Outline each Plasmodium malariae-infected red blood cell.
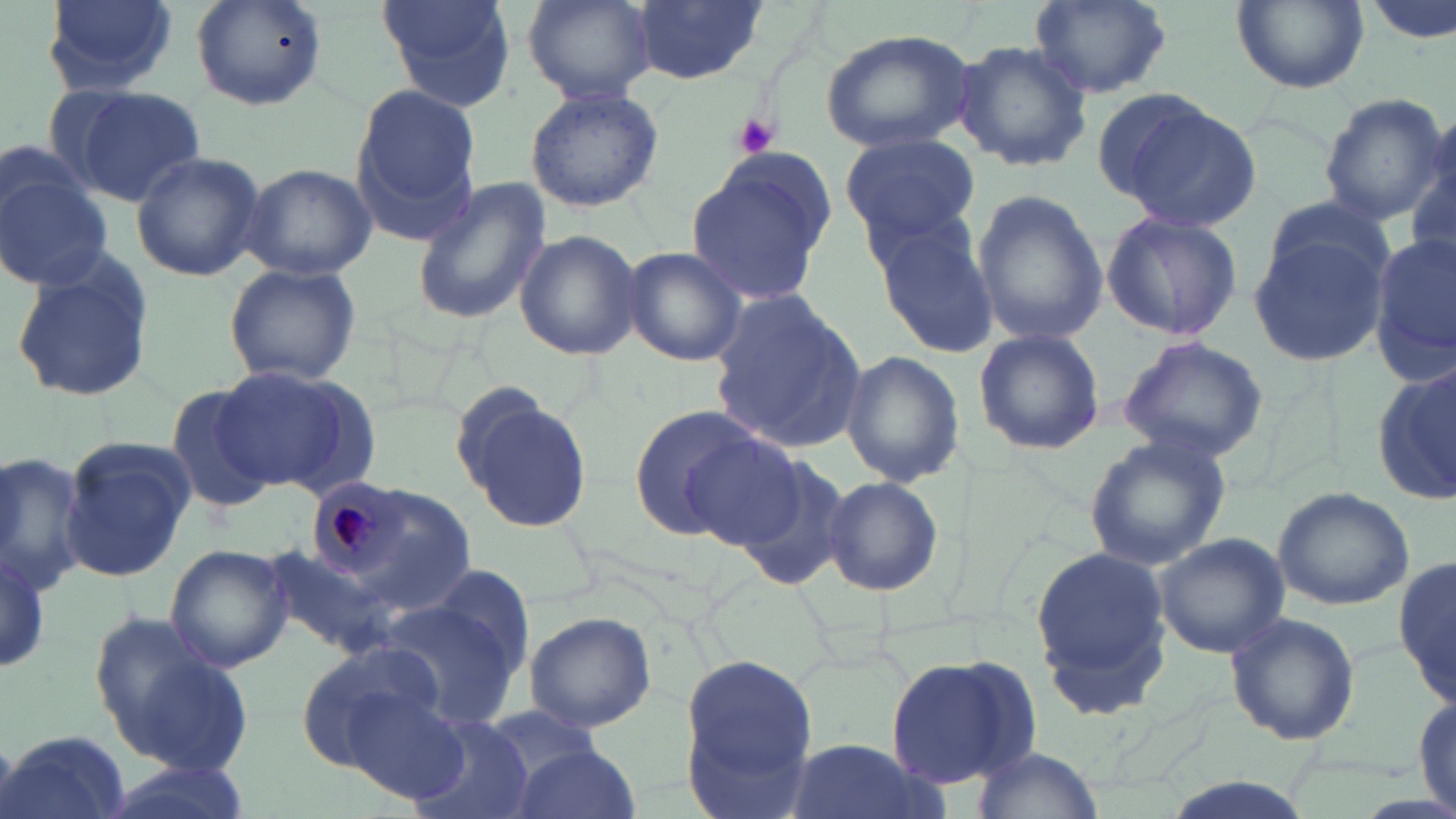
Approximate bounding boxes as [x1, y1, x2, y2] in pixels.
Plasmodium malariae-infected red blood cells: [306, 476, 409, 578].

Uninfected red blood cell locations: [39, 0, 183, 95], [187, 0, 330, 112], [376, 0, 515, 111], [522, 0, 655, 104], [630, 0, 766, 84], [1029, 0, 1171, 98], [1231, 0, 1366, 94], [1365, 0, 1456, 48], [819, 28, 977, 153], [952, 40, 1093, 173], [350, 83, 479, 244], [64, 84, 206, 207], [524, 86, 665, 213], [1316, 91, 1446, 226], [1113, 96, 1262, 231], [842, 132, 981, 242], [1410, 133, 1456, 267], [130, 151, 267, 283], [0, 152, 115, 292], [684, 162, 829, 309], [241, 164, 377, 280], [410, 177, 552, 327], [968, 187, 1108, 349], [1101, 210, 1243, 342], [866, 211, 998, 358], [1247, 218, 1391, 367], [512, 229, 642, 361], [1370, 234, 1456, 376], [621, 245, 748, 365], [9, 253, 155, 406], [222, 262, 363, 389], [709, 291, 869, 454], [973, 328, 1106, 457], [1115, 335, 1273, 463], [839, 350, 965, 487], [1373, 361, 1455, 507], [213, 366, 375, 497], [159, 384, 283, 513], [453, 385, 595, 534], [628, 404, 778, 541], [678, 431, 809, 550], [1083, 433, 1233, 572], [60, 438, 194, 582], [0, 448, 91, 598], [734, 456, 855, 593], [821, 475, 944, 597], [1270, 486, 1414, 611], [342, 487, 474, 608], [1153, 533, 1290, 657], [1028, 539, 1173, 720], [0, 541, 52, 673], [164, 544, 296, 673], [1394, 552, 1454, 709], [422, 562, 537, 681], [379, 595, 525, 732], [1224, 610, 1360, 746], [522, 611, 656, 733], [91, 616, 252, 773], [295, 640, 448, 769], [678, 653, 821, 807], [886, 654, 1034, 791], [343, 687, 473, 804], [1412, 692, 1455, 816], [480, 705, 604, 789], [404, 715, 538, 819], [1, 729, 133, 819], [775, 738, 951, 819], [507, 744, 639, 819], [971, 745, 1104, 818]. Platelet locations: [728, 113, 782, 160]. Slide-level diagnosis: Plasmodium malariae. Thin blood smear. Image is 1456×819 pixels. Light microscopy. Single field of view. May-Grünwald-Giemsa-stained preparation. Captured at 1000x magnification.